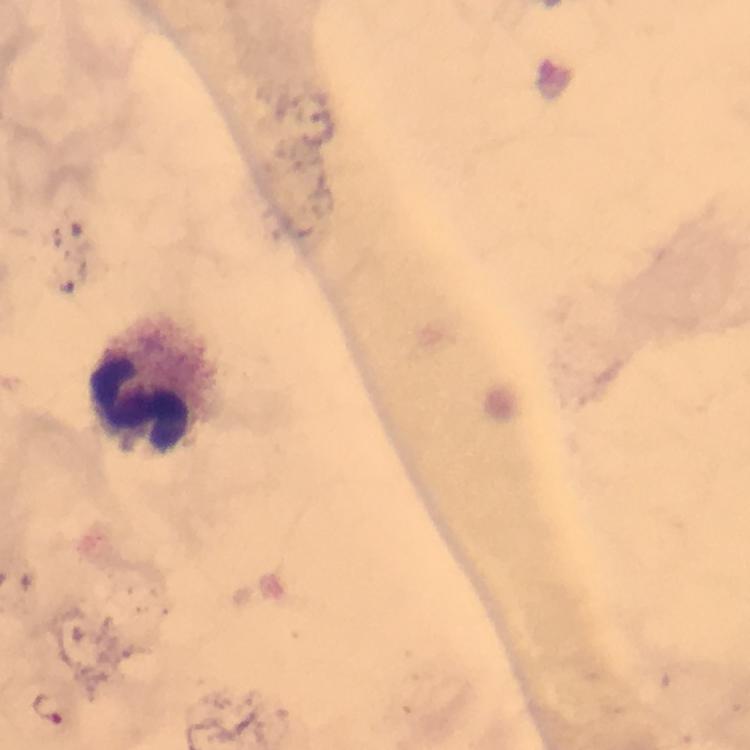
Approximate centers as {x, y} in pixels. Leukocyte locations: {147, 386}. Image is 750×750 pixels. Thick smear. Giemsa-stained preparation. Photographed through the microscope with a smartphone camera. Immersion oil was used. From a malaria diagnostic workup. At 100x magnification. Malaria parasites: none seen. Cropped region of a single field of view.